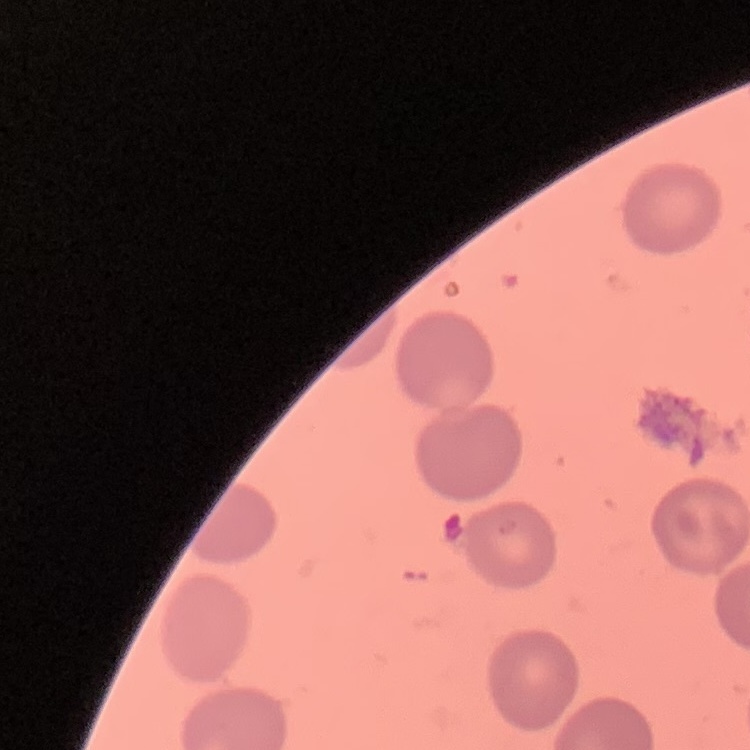
red blood cell morphology = no rouleaux formation
image type = square crop of a larger photomicrograph
stain = Field's or Giemsa
preparation = thin blood film